Evaluate for malaria.
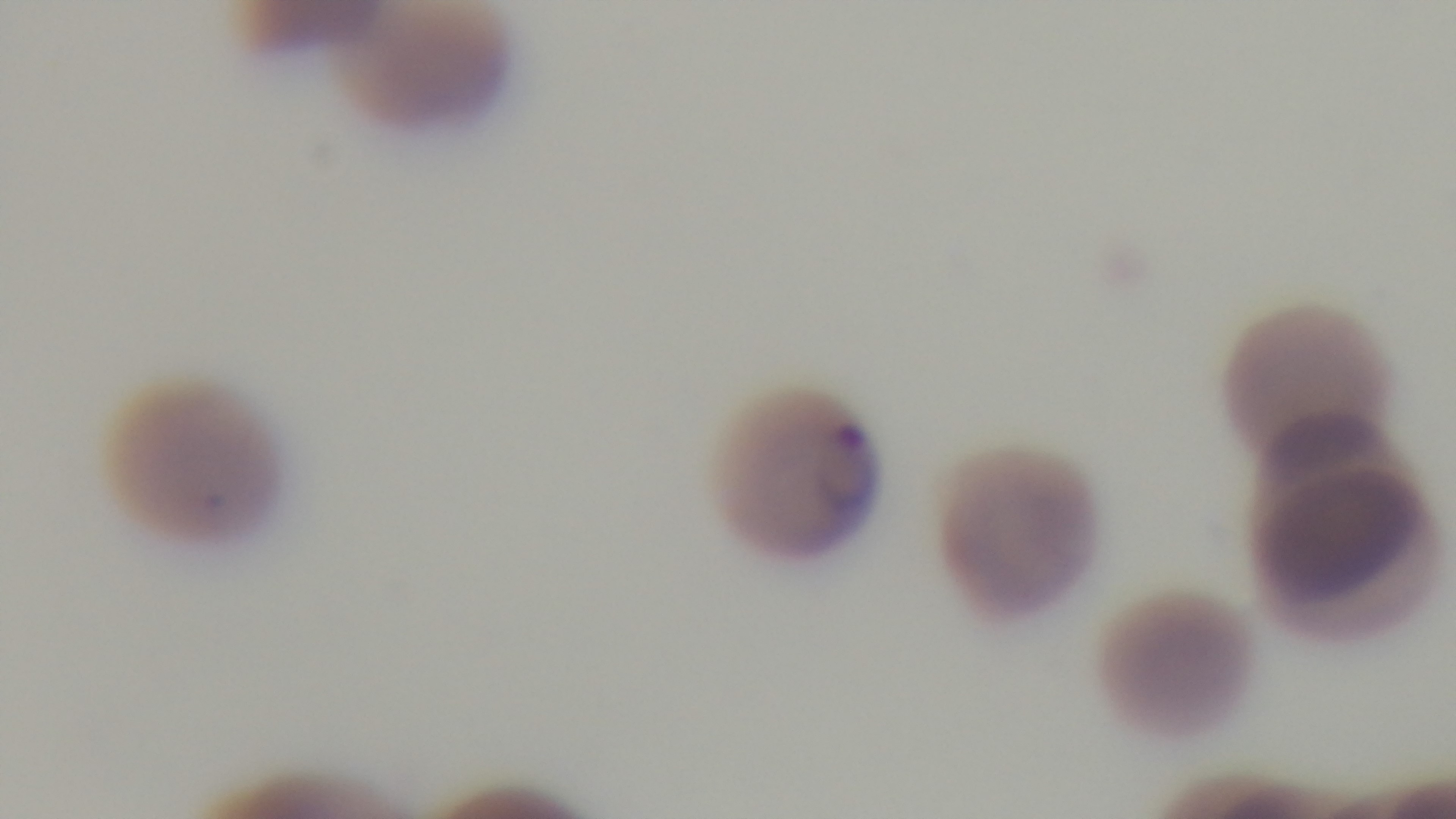
Positive.

modality: light microscopy
capture: mounted 4K digital camera
preparation: thin smear
objective: 100x oil immersion
stain: Giemsa
field_of_view: single